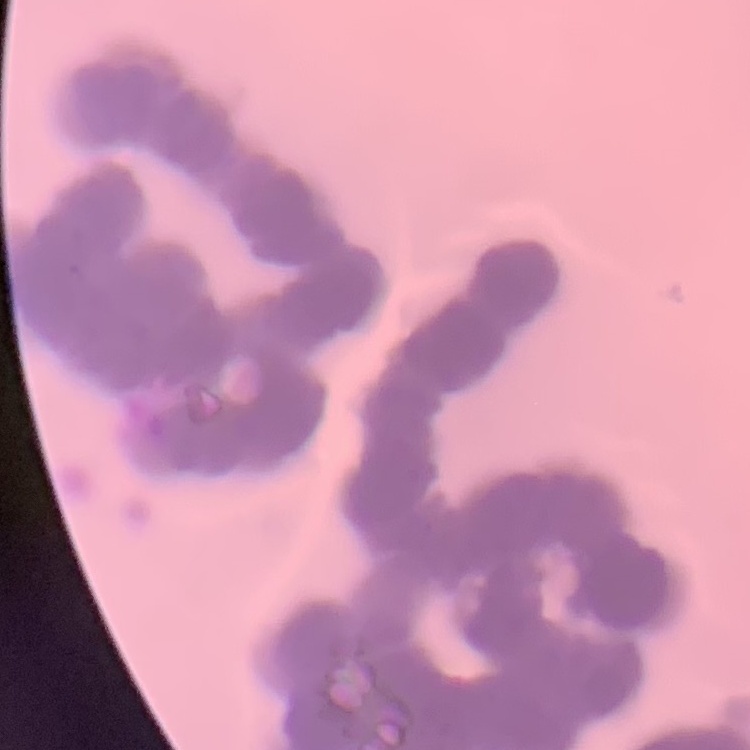 The red blood cells exhibit rouleaux formation. Field's or Giemsa stain. Thin peripheral smear. Square crop of a larger photomicrograph.